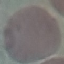

Summary:
  - Result: no malaria parasites detected
  - Image type: automatically extracted cell patch, resized to 64 × 64 pixels
  - Stain: Giemsa
  - Preparation: thin blood film
  - Capture: smartphone through the microscope eyepiece